Comment on the morphology of the erythrocytes.
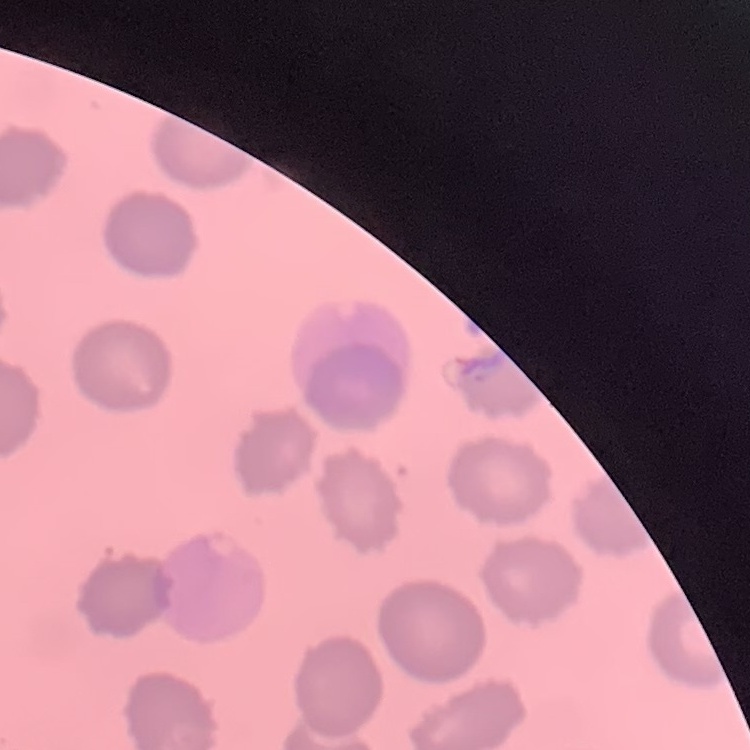
No rouleaux formation.

Thin blood film. Square crop of a larger photomicrograph. Stained with either Field's or Giemsa.